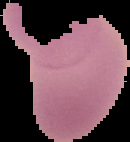

preparation: thin blood film
malaria_status: uninfected
image_size: 130×142 pixels
image_type: segmented cell region on a black background